Outline each Plasmodium falciparum-infected red blood cell.
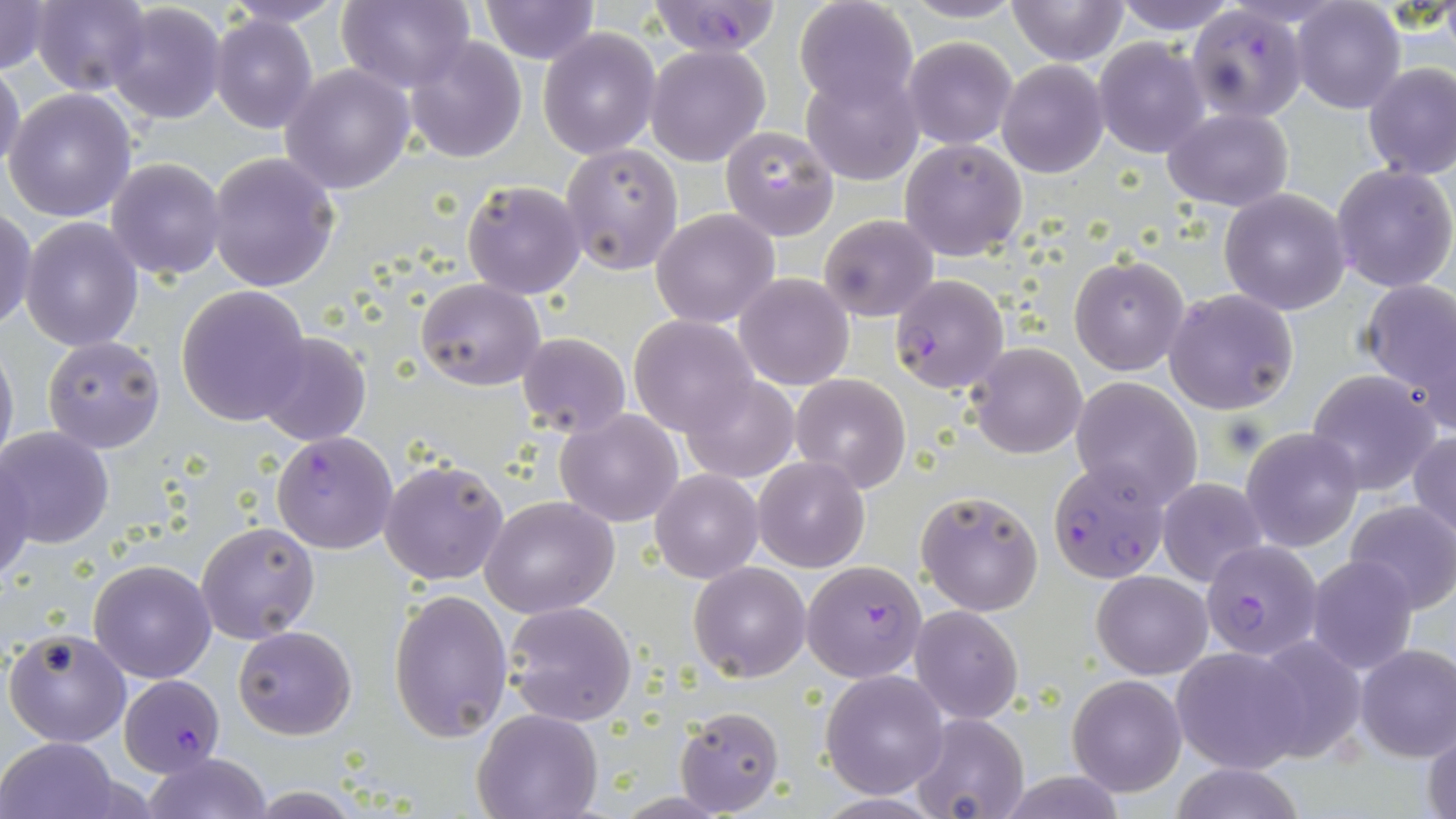

Approximate bounding boxes as named x1/y1/x2/y2 corners in pixels.
Plasmodium falciparum-infected red blood cells: (x1=644, y1=0, x2=782, y2=57), (x1=1184, y1=7, x2=1307, y2=122), (x1=890, y1=273, x2=1009, y2=394), (x1=272, y1=431, x2=398, y2=555), (x1=1045, y1=463, x2=1171, y2=583), (x1=1200, y1=539, x2=1323, y2=660), (x1=800, y1=561, x2=928, y2=683), (x1=118, y1=672, x2=228, y2=776).

Uninfected red blood cell locations: (x1=28, y1=0, x2=151, y2=94), (x1=337, y1=0, x2=478, y2=92), (x1=479, y1=0, x2=601, y2=65), (x1=793, y1=0, x2=919, y2=114), (x1=896, y1=0, x2=1028, y2=24), (x1=1006, y1=0, x2=1130, y2=66), (x1=1109, y1=0, x2=1242, y2=34), (x1=0, y1=1, x2=53, y2=76), (x1=215, y1=1, x2=353, y2=27), (x1=1293, y1=2, x2=1405, y2=114), (x1=106, y1=4, x2=225, y2=125), (x1=210, y1=13, x2=318, y2=132), (x1=537, y1=26, x2=661, y2=159), (x1=902, y1=34, x2=1018, y2=149), (x1=405, y1=36, x2=528, y2=162), (x1=1093, y1=38, x2=1212, y2=156), (x1=644, y1=44, x2=771, y2=167), (x1=996, y1=60, x2=1109, y2=178), (x1=0, y1=61, x2=25, y2=176), (x1=280, y1=63, x2=417, y2=194), (x1=1362, y1=63, x2=1456, y2=182), (x1=801, y1=68, x2=923, y2=185), (x1=3, y1=89, x2=138, y2=222), (x1=1162, y1=107, x2=1294, y2=210), (x1=719, y1=125, x2=840, y2=240), (x1=901, y1=138, x2=1028, y2=260), (x1=561, y1=144, x2=684, y2=275), (x1=206, y1=151, x2=341, y2=292), (x1=106, y1=157, x2=228, y2=279), (x1=1330, y1=163, x2=1456, y2=293), (x1=462, y1=179, x2=585, y2=299), (x1=1218, y1=188, x2=1351, y2=314), (x1=651, y1=209, x2=780, y2=328), (x1=0, y1=210, x2=37, y2=331), (x1=818, y1=213, x2=939, y2=322), (x1=20, y1=217, x2=144, y2=353), (x1=1070, y1=254, x2=1190, y2=375), (x1=734, y1=274, x2=855, y2=391), (x1=415, y1=277, x2=546, y2=390), (x1=1357, y1=279, x2=1456, y2=414), (x1=175, y1=286, x2=312, y2=426), (x1=1163, y1=289, x2=1299, y2=414), (x1=629, y1=315, x2=759, y2=437), (x1=253, y1=331, x2=371, y2=447), (x1=517, y1=332, x2=630, y2=437), (x1=42, y1=336, x2=165, y2=455), (x1=0, y1=340, x2=18, y2=474), (x1=967, y1=342, x2=1088, y2=458), (x1=1306, y1=368, x2=1441, y2=495), (x1=679, y1=373, x2=799, y2=483), (x1=789, y1=374, x2=911, y2=491), (x1=1070, y1=377, x2=1202, y2=508), (x1=556, y1=408, x2=684, y2=528), (x1=0, y1=429, x2=114, y2=549), (x1=1241, y1=429, x2=1363, y2=551), (x1=1409, y1=432, x2=1456, y2=541), (x1=2, y1=457, x2=35, y2=585), (x1=753, y1=457, x2=868, y2=572), (x1=379, y1=458, x2=511, y2=587), (x1=650, y1=469, x2=763, y2=582), (x1=1157, y1=476, x2=1267, y2=588), (x1=916, y1=489, x2=1043, y2=617), (x1=480, y1=495, x2=621, y2=618), (x1=1344, y1=501, x2=1456, y2=613), (x1=195, y1=521, x2=320, y2=644), (x1=1305, y1=554, x2=1419, y2=675), (x1=87, y1=558, x2=217, y2=683), (x1=689, y1=561, x2=812, y2=682), (x1=1092, y1=570, x2=1212, y2=678), (x1=389, y1=588, x2=513, y2=741), (x1=503, y1=600, x2=637, y2=726), (x1=909, y1=605, x2=1023, y2=724), (x1=233, y1=625, x2=357, y2=740), (x1=3, y1=627, x2=131, y2=748), (x1=1245, y1=631, x2=1369, y2=764), (x1=1355, y1=644, x2=1456, y2=761), (x1=1172, y1=646, x2=1310, y2=773), (x1=820, y1=670, x2=950, y2=797), (x1=1067, y1=675, x2=1186, y2=796), (x1=674, y1=705, x2=784, y2=816), (x1=472, y1=709, x2=604, y2=819), (x1=910, y1=713, x2=1029, y2=819), (x1=1423, y1=722, x2=1456, y2=819), (x1=0, y1=737, x2=125, y2=819), (x1=142, y1=752, x2=269, y2=819), (x1=1169, y1=762, x2=1307, y2=819), (x1=998, y1=774, x2=1130, y2=817). Slide-level diagnosis: Plasmodium falciparum. 1000x magnification. Image is 1456×819 pixels. Thin blood smear. May-Grünwald-Giemsa-stained preparation. Optical microscopy. One field of a larger specimen.